Classify this cell by malaria status.
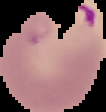

It is parasitized.

{
  "image_size": "106×112 pixels",
  "image_type": "segmented cell region with the area outside set to black",
  "preparation": "thin blood film"
}